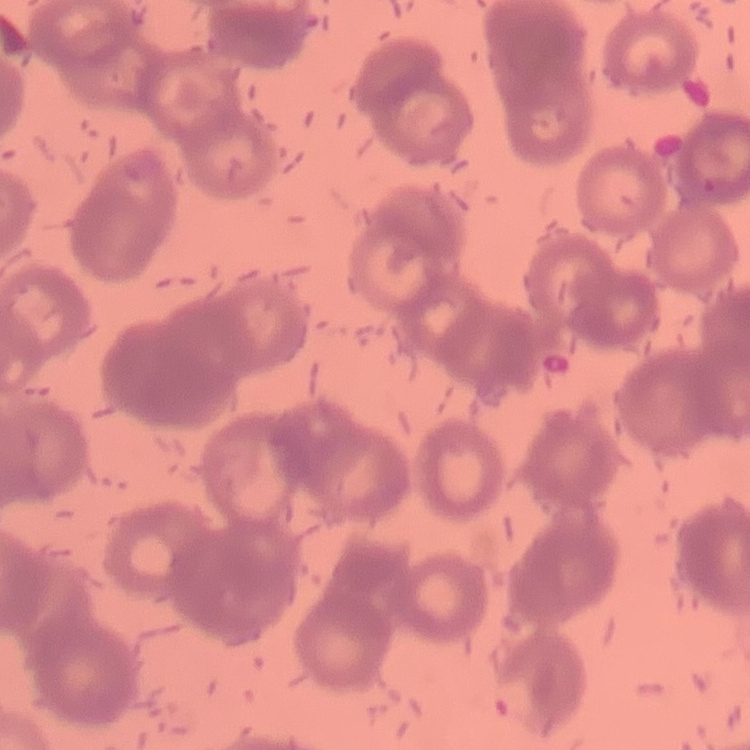 The red blood cells show rouleaux formation. Field's or Giemsa stain. Thin blood film. One tile cut from a larger photomicrograph.